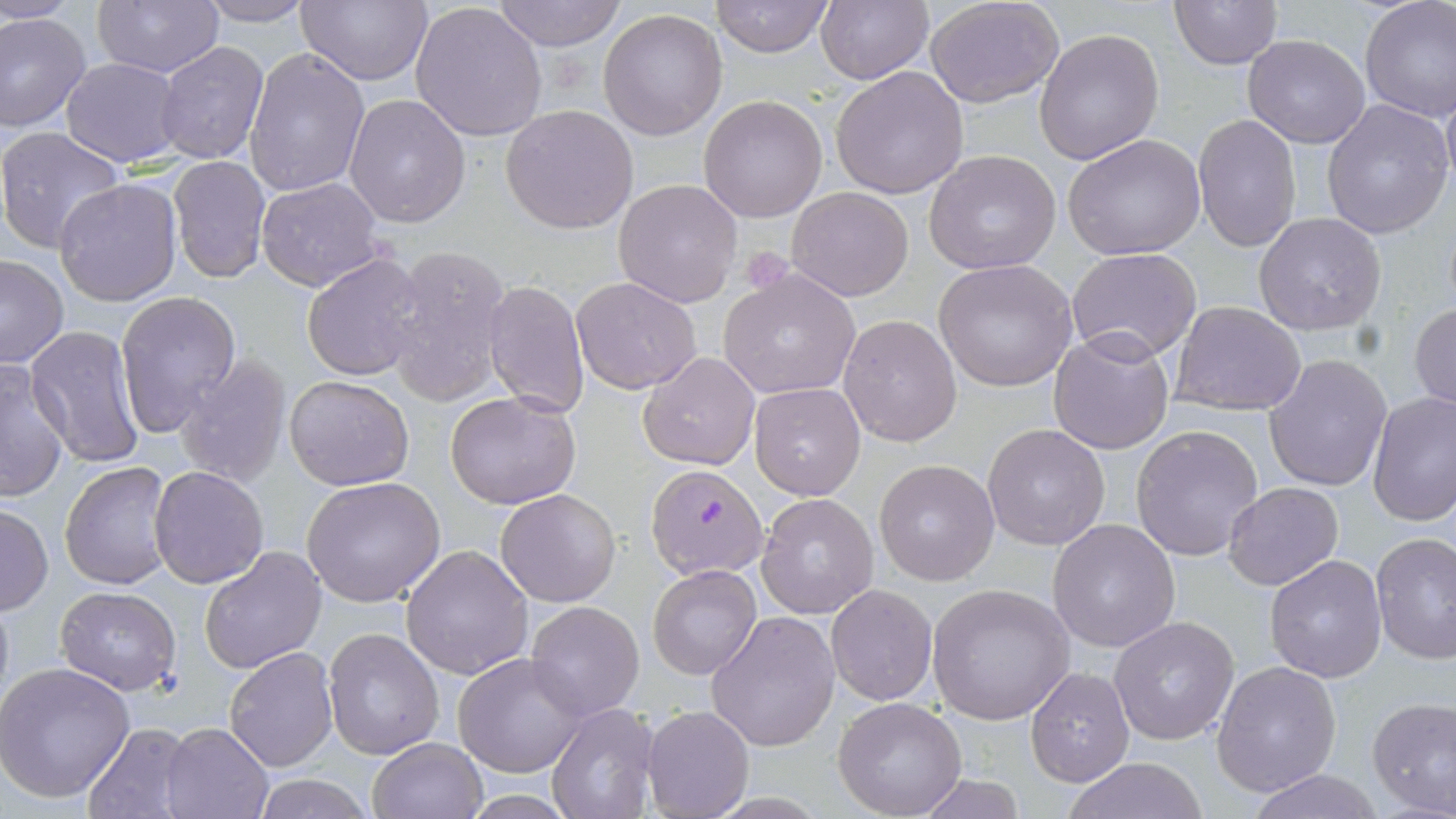
slide-level diagnosis = Plasmodium falciparum
image size = 1456×819 pixels
platelet locations = approximate bounding boxes as (x1,y1)-(x2,y2) corner pairs in pixels: (738,245)-(793,291)
field of view = one of a larger specimen
modality = optical microscopy
stain = May-Grünwald-Giemsa
uninfected red blood cell locations = approximate bounding boxes as (x1,y1)-(x2,y2) corner pairs in pixels: (2,0)-(82,24), (91,0)-(224,79), (295,0)-(433,87), (408,0)-(550,143), (492,0)-(625,51), (711,0)-(832,57), (816,0)-(933,85), (1358,0)-(1456,122), (924,1)-(1066,109), (1169,1)-(1282,70), (197,2)-(318,26), (597,8)-(729,142), (0,11)-(91,134), (1033,27)-(1163,164), (1242,35)-(1370,149), (155,41)-(270,166), (244,47)-(369,197), (61,56)-(184,166), (830,65)-(969,199), (1440,78)-(1456,196), (344,93)-(472,229), (698,93)-(828,224), (1321,99)-(1453,240), (501,103)-(638,233), (1193,112)-(1301,252), (0,127)-(128,255), (1062,132)-(1208,260), (923,150)-(1062,275), (167,155)-(272,285), (256,176)-(386,292), (54,177)-(182,305), (613,178)-(744,308), (785,186)-(913,301), (1253,211)-(1388,335), (383,243)-(515,406), (1067,247)-(1204,364), (300,251)-(428,382), (0,254)-(69,369), (932,258)-(1080,393), (718,269)-(863,400), (570,275)-(702,394), (483,281)-(592,418), (114,291)-(241,437), (1410,300)-(1456,413), (1169,301)-(1306,416), (838,314)-(965,448), (24,325)-(148,471), (1047,330)-(1176,456), (638,351)-(762,472), (1264,353)-(1393,491), (172,355)-(293,489), (0,363)-(71,501), (284,374)-(414,491), (750,382)-(867,499), (445,389)-(583,510), (1367,391)-(1455,526), (983,423)-(1111,551), (1130,424)-(1265,562), (875,459)-(1000,586), (59,460)-(176,591), (150,465)-(271,588), (302,477)-(447,607), (1222,482)-(1344,590), (496,488)-(620,607), (755,492)-(879,618), (0,504)-(52,615), (1047,517)-(1182,652), (1371,532)-(1456,665), (401,544)-(534,681), (199,546)-(328,674), (1264,554)-(1386,683), (646,565)-(761,681), (928,583)-(1074,725), (826,584)-(938,704), (53,586)-(182,696), (525,601)-(644,719), (704,610)-(840,751), (1109,614)-(1239,743), (323,626)-(447,761), (224,647)-(338,770), (454,652)-(589,777), (1211,660)-(1342,798), (0,661)-(135,804), (1025,666)-(1135,786), (1366,696)-(1456,819), (831,697)-(969,818), (547,703)-(662,819), (643,704)-(753,816), (160,721)-(273,819), (79,723)-(196,819), (366,736)-(488,819), (1061,757)-(1212,818), (1242,770)-(1387,819), (249,773)-(376,818), (910,774)-(1029,817)
preparation = thin blood film
Plasmodium falciparum-infected red blood cell locations = approximate bounding boxes as (x1,y1)-(x2,y2) corner pairs in pixels: (647,463)-(768,580)
magnification = 1000x